Assess this cell for malaria.
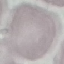
It is uninfected.

{
  "image_type": "cell patch, automatically extracted from a larger field of view and resized to 64 × 64 pixels",
  "preparation": "thin blood smear",
  "stain": "Giemsa",
  "capture": "smartphone camera at the microscope eyepiece"
}